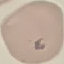 Malaria status: uninfected. Cell patch, automatically extracted from a larger field of view and resized to 64 × 64 pixels. Giemsa-stained preparation. Thin blood smear. Photographed with a smartphone camera at the microscope eyepiece.